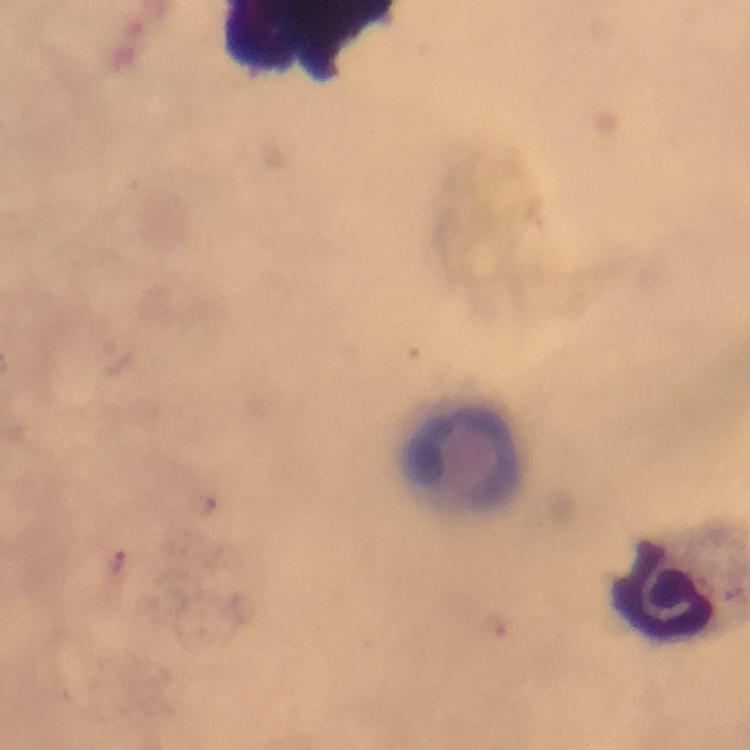

magnification = 100x
image size = 750×750 pixels
capture = smartphone camera through the microscope
context = from a diagnostic examination for malaria
immersion oil = used
preparation = thick smear
cropped from = one field of view
stain = Giemsa
leukocyte locations = approximate centers as {x, y} in pixels: {458, 454}
malaria parasite locations = approximate centers as {x, y} in pixels: {119, 564}